State which parasite is depicted.
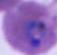

Plasmodium.

magnification = 400x or 1000x
modality = photomicrograph